Describe the morphology of the red blood cells.
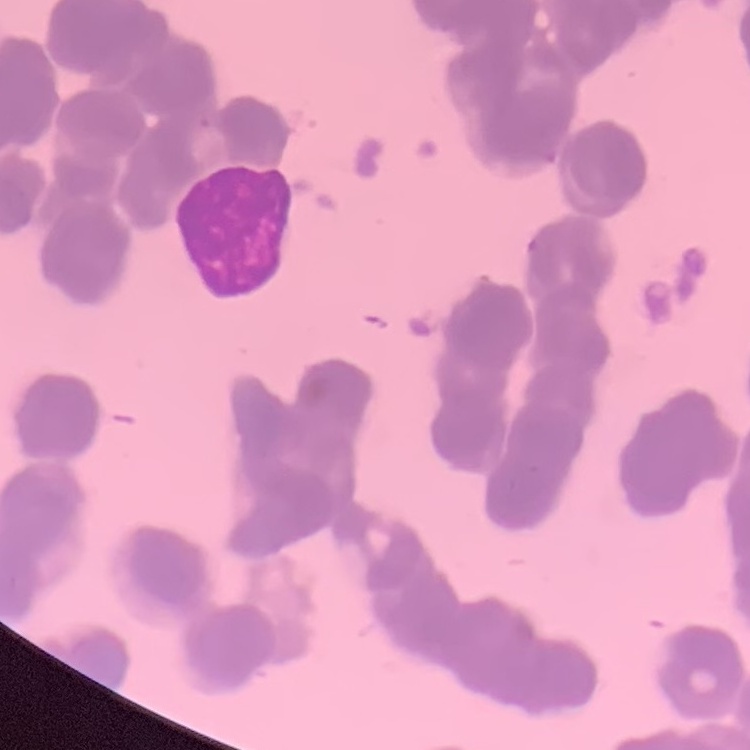

Rouleaux formation.

image type = square crop of a larger photomicrograph
preparation = thin blood smear
stain = Field's or Giemsa